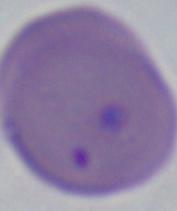

Summary:
  - Modality: micrograph
  - Magnification: 1000x
  - Identification: Babesia